Outline each blood parasite and name the species.
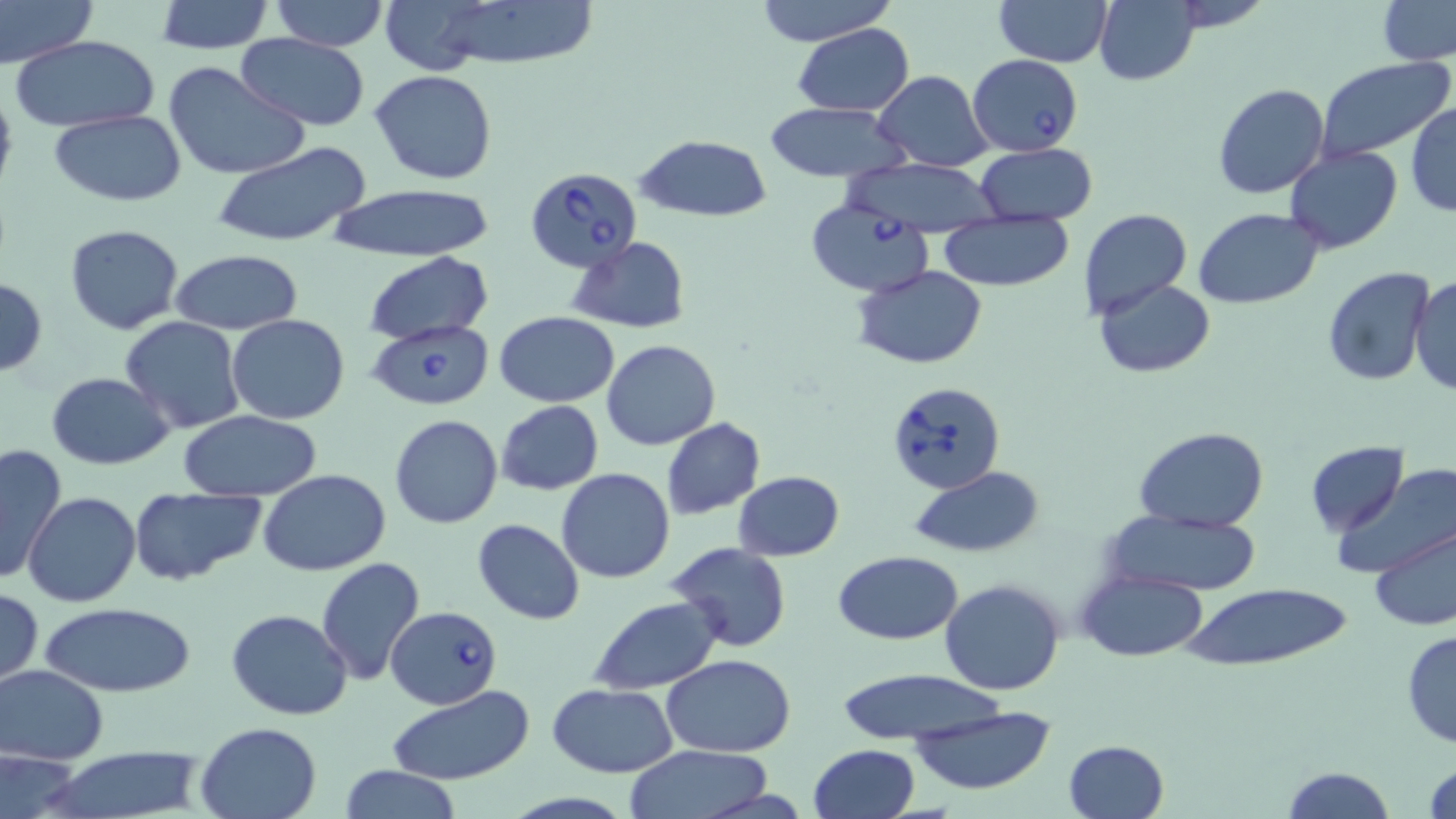
Approximate bounding boxes as (x1,y1)-(x2,y2) corner pairs in pixels.
Babesia divergens-infected red blood cells: (967,53)-(1084,155), (524,167)-(642,273), (806,199)-(932,295), (364,318)-(496,411), (884,380)-(1006,494), (387,605)-(501,710).
No Plasmodium falciparum, Plasmodium ovale, Plasmodium malariae, Plasmodium vivax, or Trypanosoma brucei observed.

Summary:
  - Uninfected red blood cell locations: (0,0)-(96,66), (268,0)-(391,50), (403,0)-(601,70), (753,0)-(898,47), (993,0)-(1112,67), (1163,0)-(1275,33), (156,1)-(273,52), (1093,1)-(1201,86), (1376,1)-(1456,65), (792,23)-(913,116), (235,34)-(369,128), (10,35)-(158,132), (1314,57)-(1455,166), (163,60)-(308,180), (872,70)-(993,171), (370,71)-(497,184), (1212,83)-(1330,199), (0,84)-(18,199), (765,102)-(910,185), (1406,102)-(1455,218), (48,111)-(188,205), (635,134)-(772,223), (212,141)-(375,249), (974,143)-(1097,226), (1282,144)-(1402,254), (842,157)-(1005,237), (326,184)-(496,263), (1194,208)-(1323,308), (1078,209)-(1191,320), (940,213)-(1074,293), (64,223)-(186,334), (566,237)-(691,333), (168,250)-(304,335), (364,251)-(493,346), (852,265)-(989,367), (1322,266)-(1434,387), (1411,273)-(1456,396), (0,279)-(47,374), (1093,279)-(1215,378), (495,312)-(620,406), (226,314)-(349,424), (120,316)-(246,434), (603,340)-(719,449), (46,372)-(176,470), (497,400)-(603,495), (177,411)-(325,502), (389,414)-(503,529), (661,417)-(766,520), (1134,427)-(1270,531), (1305,440)-(1407,537), (0,443)-(67,583), (1339,465)-(1455,577), (909,467)-(1043,558), (556,468)-(675,583), (259,470)-(391,575), (732,471)-(843,560), (130,487)-(265,587), (23,492)-(140,607), (1100,510)-(1262,595), (473,518)-(585,625), (1370,524)-(1456,633), (664,543)-(793,653), (834,549)-(964,645), (315,557)-(426,686), (1077,569)-(1209,661), (940,578)-(1067,696), (1183,583)-(1351,671), (0,586)-(43,688), (589,595)-(724,695), (39,600)-(194,697), (227,608)-(353,719), (1401,629)-(1456,748), (661,654)-(797,756), (0,664)-(109,764), (834,668)-(1009,745), (546,683)-(677,778), (387,687)-(536,783), (907,702)-(1058,798), (195,721)-(323,818), (1062,739)-(1169,819), (810,742)-(921,819), (622,745)-(776,819), (44,747)-(206,819), (0,750)-(85,818), (1423,757)-(1455,818), (337,765)-(464,819), (1278,766)-(1397,819)
  - Slide-level diagnosis: Babesia divergens
  - Preparation: thin blood smear
  - Stain: May-Grünwald-Giemsa
  - Image size: 1456×819 pixels
  - Magnification: 1000x
  - Field of view: single
  - Modality: optical microscopy